Give the preparation type.
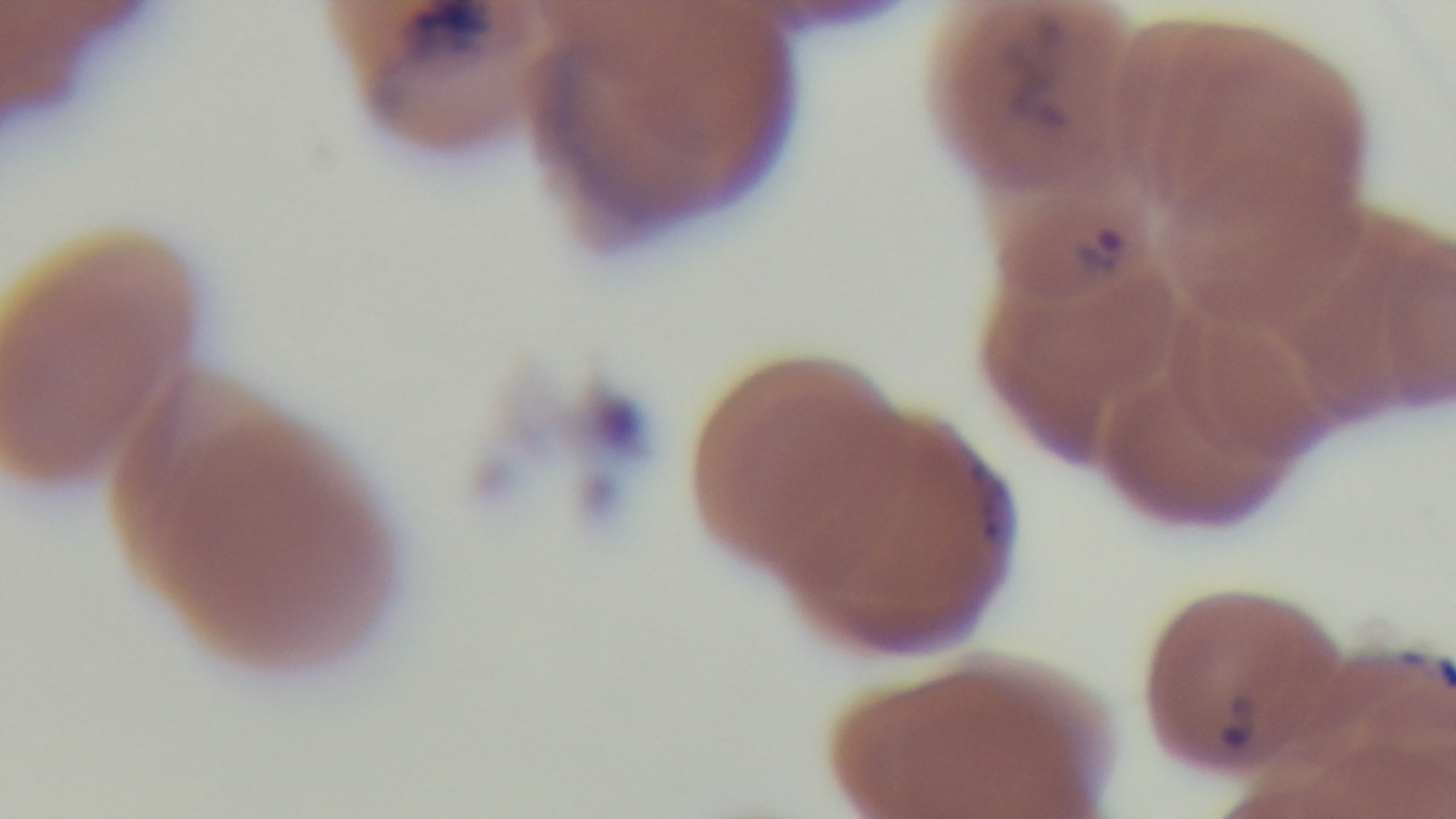
It is a thin blood film.

capture: mounted 4K digital camera
malaria_status: infected
stain: Giemsa
modality: light microscopy
objective: 100x oil immersion
field_of_view: single